Give the extent of all uninfected red blood cells.
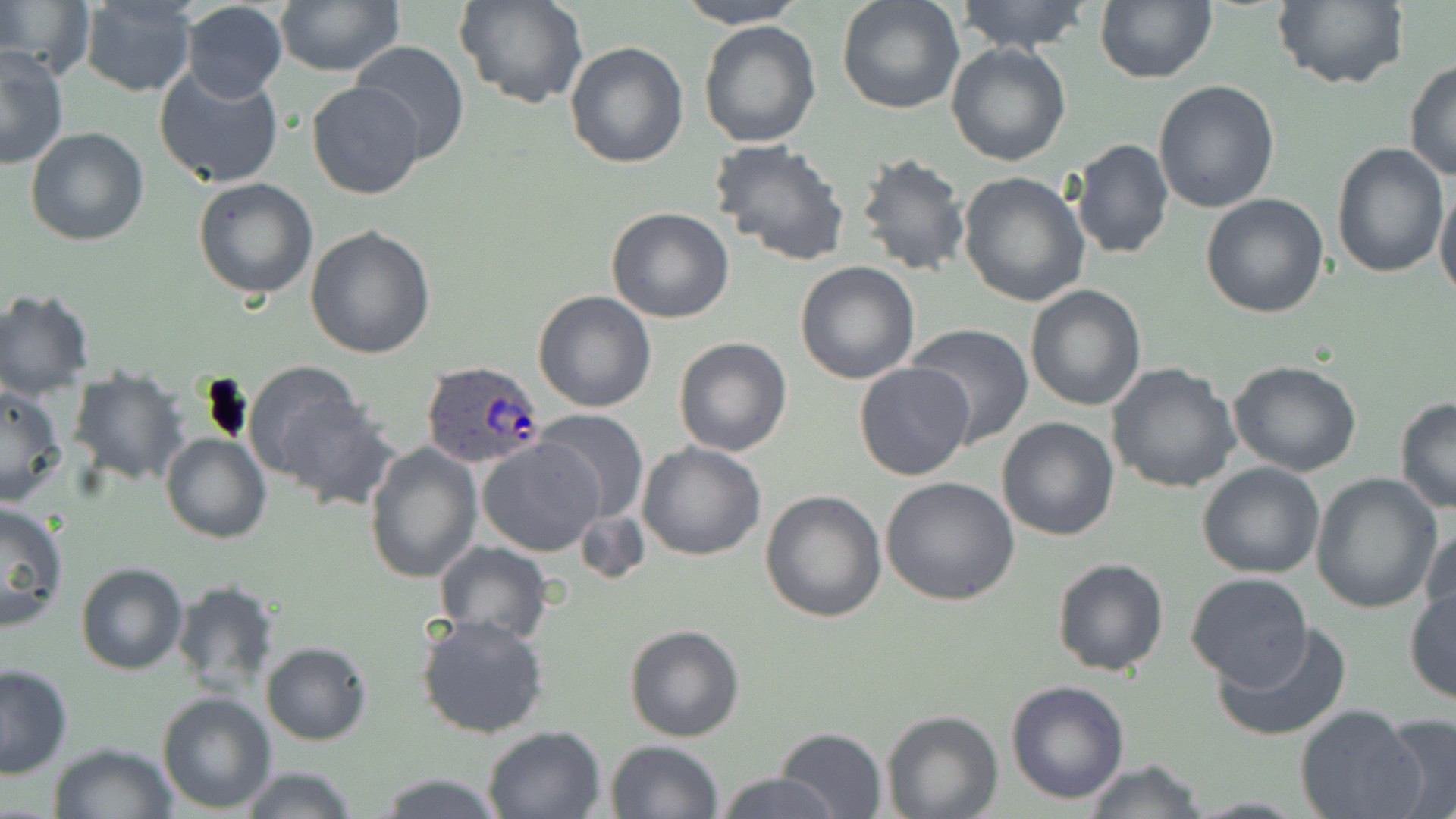

Approximate bounding boxes as (x1,y1)-(x2,y2) corner pairs in pixels.
Uninfected red blood cells: (458,0)-(587,110), (674,0)-(807,29), (836,0)-(965,116), (953,0)-(1095,54), (1094,0)-(1217,84), (1271,0)-(1406,90), (0,1)-(90,78), (78,1)-(197,96), (274,1)-(402,76), (179,2)-(288,103), (698,20)-(822,149), (348,41)-(472,166), (564,42)-(689,169), (947,43)-(1073,166), (0,46)-(69,169), (1404,61)-(1456,183), (153,63)-(286,189), (307,80)-(425,200), (1152,80)-(1281,214), (26,126)-(148,247), (709,137)-(851,266), (1070,139)-(1173,259), (1331,145)-(1449,281), (855,151)-(973,279), (958,172)-(1091,307), (193,177)-(318,299), (1434,184)-(1456,301), (1199,193)-(1330,318), (605,207)-(735,323), (305,225)-(437,360), (795,261)-(922,384), (1025,285)-(1148,411), (0,287)-(96,399), (533,290)-(656,412), (905,324)-(1033,445), (673,337)-(791,456), (1228,361)-(1363,477), (853,362)-(975,482), (1107,362)-(1240,494), (243,365)-(373,498), (68,366)-(190,486), (0,384)-(67,506), (1393,397)-(1456,512), (534,410)-(650,525), (996,417)-(1122,540), (161,432)-(270,543), (478,438)-(602,555), (365,439)-(483,583), (637,441)-(767,561), (1197,462)-(1325,580), (1310,474)-(1443,613), (880,476)-(1022,608), (760,489)-(886,623), (0,499)-(70,630), (574,507)-(649,585), (1420,524)-(1455,637), (433,540)-(554,643), (1051,557)-(1170,677), (76,562)-(188,675), (1184,572)-(1313,690), (171,579)-(280,698), (1404,586)-(1455,706), (416,613)-(551,740), (1214,619)-(1353,741), (624,624)-(745,742), (261,641)-(372,746), (0,664)-(73,778), (1005,680)-(1130,805), (157,692)-(276,813), (1296,706)-(1426,819), (880,710)-(1003,819), (1379,714)-(1456,819), (480,725)-(605,818), (773,727)-(888,818), (605,739)-(725,819), (47,741)-(178,819), (1082,759)-(1207,819), (237,766)-(362,819), (716,771)-(839,818), (372,772)-(509,818).

Summary:
  - Plasmodium ovale-infected red blood cell locations: (419,360)-(544,472)
  - Slide-level diagnosis: Plasmodium ovale
  - Field of view: single
  - Modality: optical microscopy
  - Stain: May-Grünwald-Giemsa
  - Magnification: 1000x
  - Image size: 1456×819 pixels
  - Preparation: thin blood film